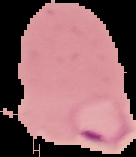
The area outside the segmented cell region is set to black. Malaria status: parasitized. From a thin blood smear. Image is 136×157 pixels.